Classify this cell by malaria status.
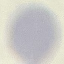

Uninfected.

{
  "capture": "smartphone through the microscope eyepiece",
  "stain": "Giemsa",
  "preparation": "thin blood film",
  "image_type": "cell patch, automatically extracted from a larger field of view and resized to 64 × 64 pixels"
}